Comment on the morphology of the erythrocytes.
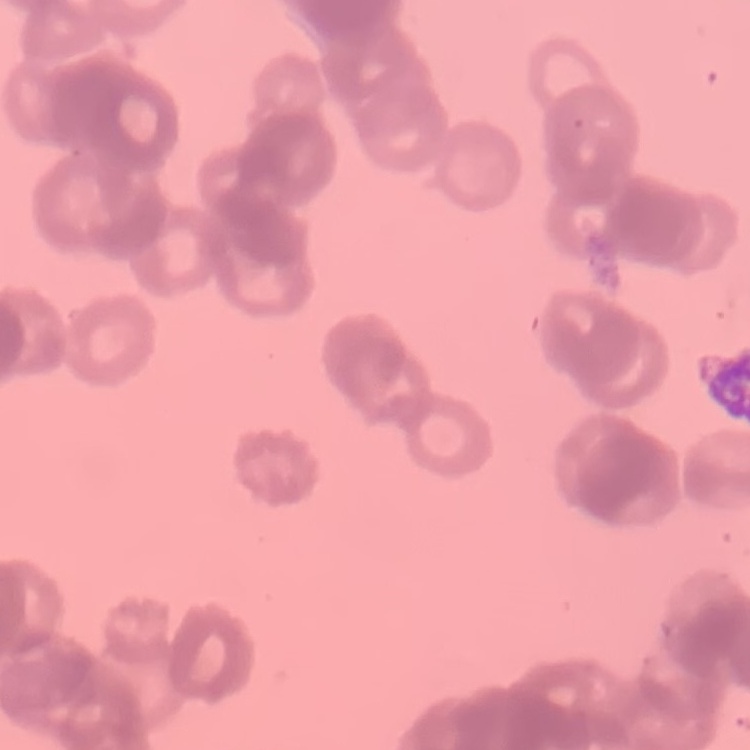

Rouleaux formation.

Thin peripheral smear. Stained with either Field's or Giemsa. One tile cut from a larger photomicrograph.